Outline platelets.
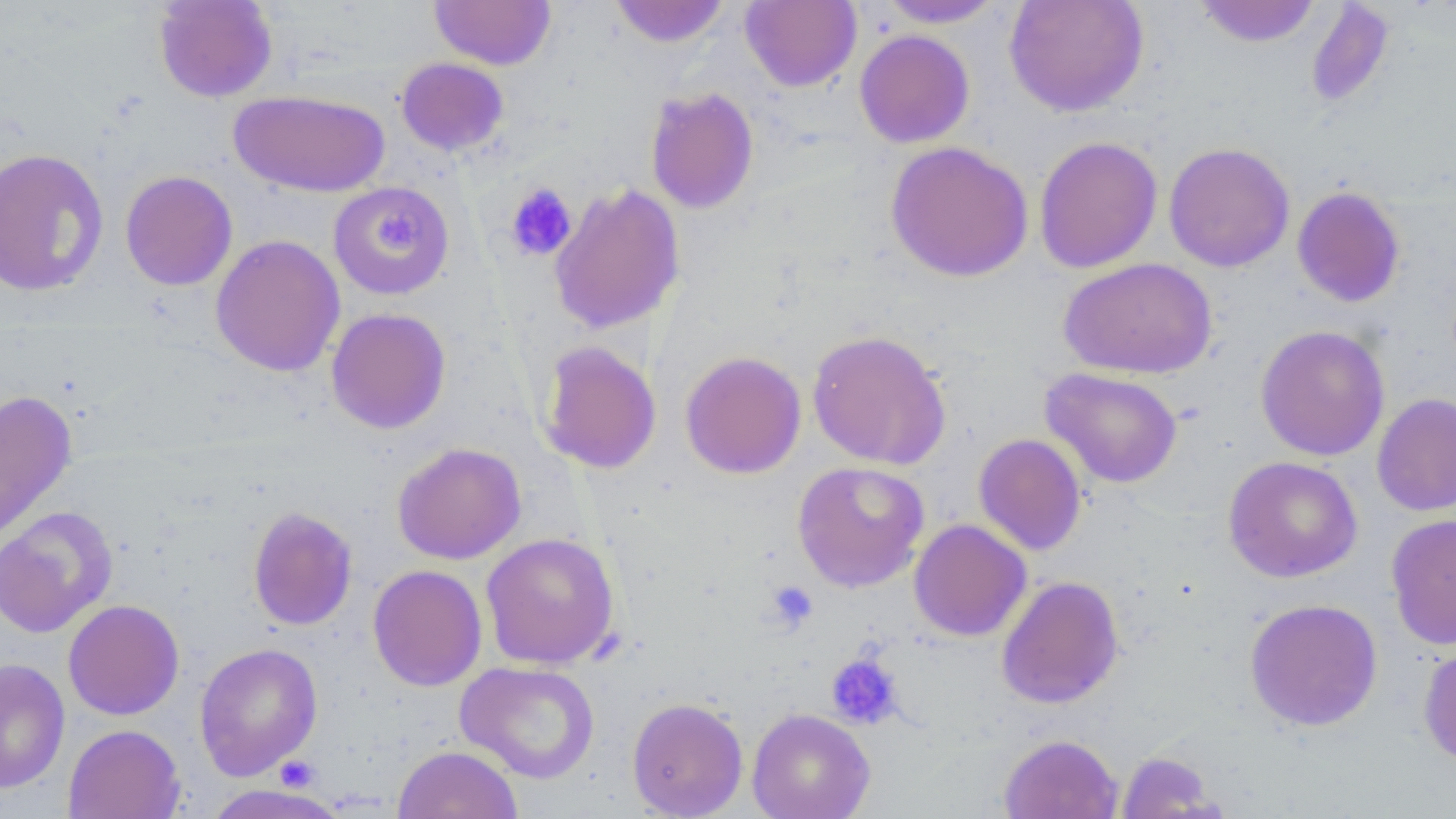
Approximate bounding boxes as [x1, y1, x2, y2] in pixels.
Platelets: [505, 183, 578, 262], [374, 208, 426, 255], [764, 580, 818, 631], [826, 653, 903, 729], [277, 754, 314, 792].

Uninfected red blood cell locations: [153, 0, 277, 103], [609, 0, 731, 48], [875, 0, 1007, 28], [1004, 0, 1149, 117], [429, 1, 556, 70], [740, 1, 861, 92], [1193, 1, 1322, 47], [1306, 2, 1396, 110], [854, 30, 975, 148], [396, 57, 509, 156], [645, 87, 759, 214], [229, 89, 390, 197], [1033, 135, 1163, 274], [884, 140, 1034, 283], [1163, 142, 1295, 272], [0, 148, 109, 298], [120, 170, 238, 291], [328, 182, 455, 300], [548, 182, 686, 334], [1291, 186, 1406, 308], [210, 234, 345, 377], [1058, 257, 1218, 380], [326, 307, 451, 434], [1255, 325, 1390, 461], [807, 329, 951, 470], [536, 340, 662, 475], [679, 350, 806, 479], [1041, 368, 1183, 488], [0, 390, 78, 543], [1372, 392, 1456, 517], [973, 433, 1087, 556], [392, 442, 526, 564], [1223, 455, 1363, 583], [792, 460, 930, 592], [0, 505, 118, 638], [247, 506, 358, 631], [1386, 513, 1456, 650], [908, 519, 1032, 642], [480, 532, 621, 669], [367, 564, 487, 691], [996, 575, 1124, 709], [1244, 598, 1383, 731], [62, 599, 184, 720], [194, 642, 323, 780], [1418, 642, 1456, 770], [0, 658, 70, 794], [456, 661, 600, 783], [626, 697, 749, 818], [747, 708, 876, 819], [63, 724, 185, 819], [998, 733, 1123, 819], [392, 745, 522, 819], [1114, 750, 1226, 818], [200, 784, 353, 819]. Slide-level diagnosis: no evidence of blood parasites. Optical microscopy. Image is 1456×819 pixels. Captured at 1000x magnification. Thin blood film. One field of a larger specimen. May-Grünwald-Giemsa stain.